Outline each blood parasite and name the species.
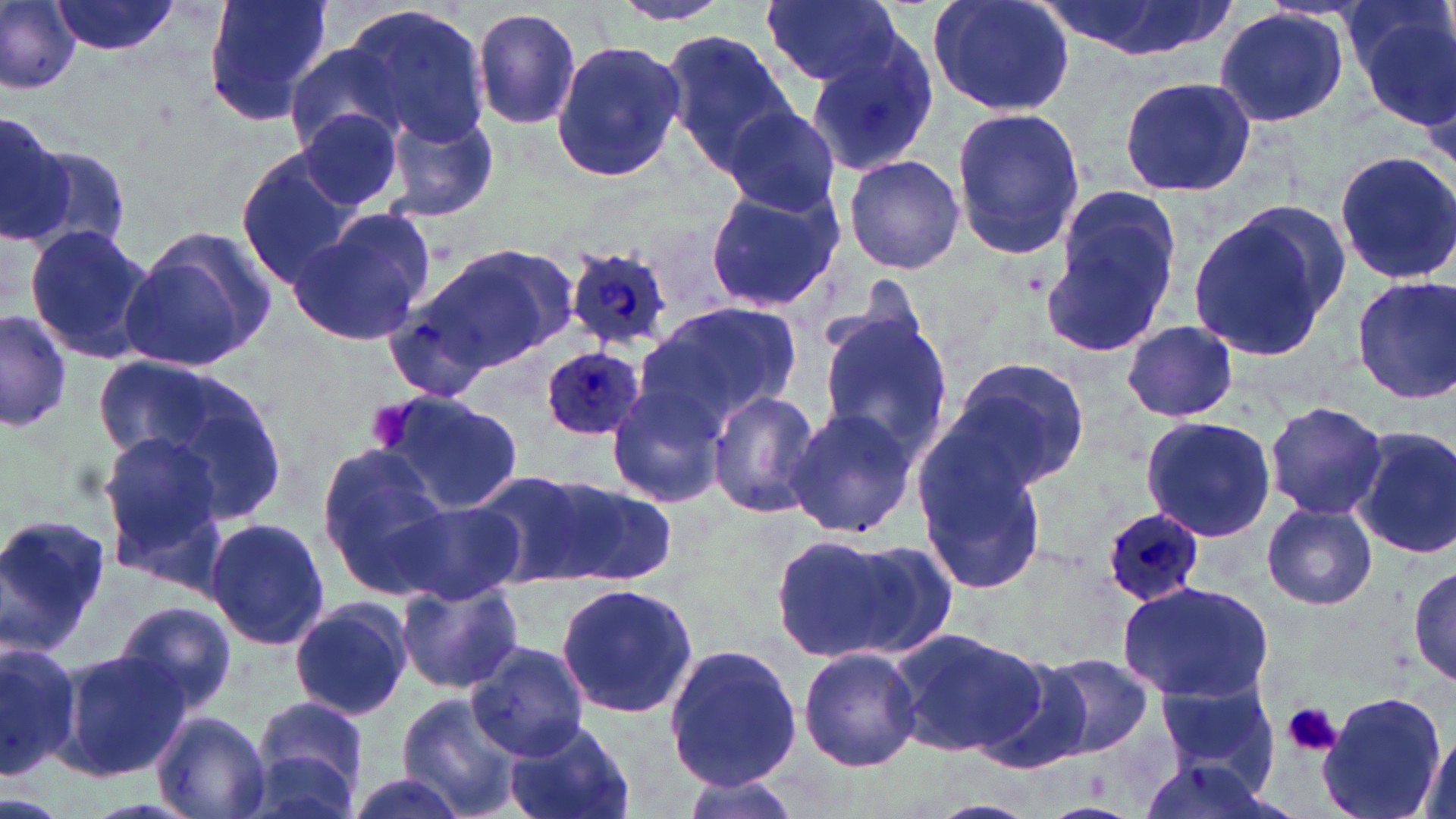
Approximate bounding boxes as named x1/y1/x2/y2 corners in pixels.
Plasmodium ovale-infected red blood cells: (x1=561, y1=242, x2=682, y2=349), (x1=537, y1=342, x2=651, y2=441), (x1=1096, y1=510, x2=1203, y2=611).
No Plasmodium falciparum, Plasmodium malariae, Plasmodium vivax, Babesia divergens, or Trypanosoma brucei observed.

Summary:
  - Platelet locations: (x1=1283, y1=701, x2=1341, y2=758)
  - Uninfected red blood cell locations: (x1=1, y1=0, x2=79, y2=93), (x1=51, y1=0, x2=185, y2=56), (x1=200, y1=0, x2=334, y2=128), (x1=605, y1=0, x2=737, y2=26), (x1=760, y1=0, x2=901, y2=87), (x1=926, y1=0, x2=1078, y2=118), (x1=1044, y1=0, x2=1228, y2=60), (x1=1345, y1=0, x2=1455, y2=121), (x1=347, y1=5, x2=491, y2=145), (x1=1210, y1=6, x2=1351, y2=129), (x1=472, y1=7, x2=583, y2=131), (x1=663, y1=29, x2=796, y2=168), (x1=803, y1=34, x2=940, y2=175), (x1=550, y1=40, x2=685, y2=182), (x1=284, y1=43, x2=410, y2=155), (x1=1118, y1=76, x2=1259, y2=197), (x1=719, y1=105, x2=843, y2=218), (x1=950, y1=106, x2=1086, y2=260), (x1=296, y1=108, x2=407, y2=217), (x1=387, y1=112, x2=500, y2=220), (x1=0, y1=113, x2=77, y2=251), (x1=21, y1=144, x2=135, y2=259), (x1=234, y1=150, x2=366, y2=287), (x1=1332, y1=151, x2=1456, y2=285), (x1=842, y1=154, x2=964, y2=275), (x1=1043, y1=184, x2=1185, y2=357), (x1=702, y1=187, x2=842, y2=312), (x1=1186, y1=202, x2=1350, y2=363), (x1=285, y1=209, x2=434, y2=349), (x1=125, y1=225, x2=281, y2=368), (x1=23, y1=226, x2=159, y2=363), (x1=406, y1=242, x2=575, y2=378), (x1=1352, y1=275, x2=1456, y2=406), (x1=635, y1=300, x2=800, y2=430), (x1=382, y1=301, x2=507, y2=405), (x1=814, y1=306, x2=953, y2=464), (x1=0, y1=307, x2=74, y2=432), (x1=1122, y1=320, x2=1239, y2=421), (x1=95, y1=352, x2=281, y2=504), (x1=948, y1=358, x2=1091, y2=490), (x1=606, y1=383, x2=726, y2=508), (x1=706, y1=387, x2=822, y2=519), (x1=373, y1=390, x2=522, y2=511), (x1=1263, y1=401, x2=1388, y2=521), (x1=785, y1=406, x2=918, y2=540), (x1=1141, y1=415, x2=1278, y2=542), (x1=1351, y1=427, x2=1456, y2=561), (x1=98, y1=433, x2=229, y2=569), (x1=912, y1=440, x2=1050, y2=595), (x1=316, y1=446, x2=454, y2=594), (x1=463, y1=466, x2=615, y2=587), (x1=527, y1=473, x2=677, y2=586), (x1=393, y1=502, x2=524, y2=604), (x1=1262, y1=503, x2=1377, y2=609), (x1=0, y1=513, x2=110, y2=655), (x1=204, y1=516, x2=330, y2=651), (x1=773, y1=532, x2=941, y2=664), (x1=1409, y1=560, x2=1456, y2=689), (x1=554, y1=580, x2=700, y2=719), (x1=397, y1=581, x2=524, y2=695), (x1=1116, y1=581, x2=1275, y2=704), (x1=289, y1=597, x2=413, y2=719), (x1=114, y1=599, x2=237, y2=715), (x1=888, y1=627, x2=1048, y2=758), (x1=0, y1=639, x2=81, y2=777), (x1=467, y1=639, x2=595, y2=760), (x1=663, y1=643, x2=801, y2=790), (x1=795, y1=645, x2=924, y2=773), (x1=58, y1=648, x2=190, y2=781), (x1=1034, y1=651, x2=1157, y2=761), (x1=974, y1=656, x2=1099, y2=775), (x1=1151, y1=676, x2=1276, y2=788), (x1=1318, y1=690, x2=1447, y2=819), (x1=394, y1=693, x2=525, y2=817), (x1=247, y1=699, x2=369, y2=812), (x1=151, y1=709, x2=270, y2=819), (x1=505, y1=719, x2=634, y2=819), (x1=1417, y1=735, x2=1455, y2=818), (x1=1133, y1=746, x2=1281, y2=819), (x1=338, y1=769, x2=480, y2=819), (x1=672, y1=771, x2=807, y2=819)
  - Slide-level diagnosis: Plasmodium ovale
  - Modality: optical microscopy
  - Preparation: thin blood smear
  - Magnification: 1000x
  - Field of view: one of a larger specimen
  - Image size: 1456×819 pixels
  - Stain: May-Grünwald-Giemsa